Report the malaria status of this cell.
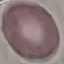

It is uninfected.

capture: smartphone camera at the microscope eyepiece
preparation: thin blood film
stain: Giemsa
image_type: automatically extracted cell patch, resized to 64 × 64 pixels